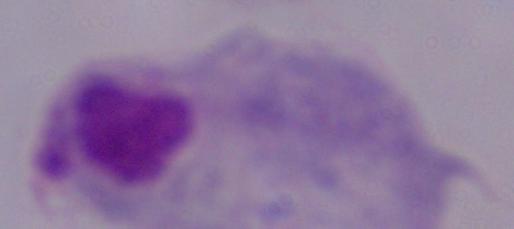
Summary:
  - Magnification: 1000x
  - Identification: trichomonad
  - Modality: micrograph